Classify this cell by malaria status.
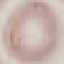
Uninfected.

{
  "stain": "Giemsa",
  "preparation": "thin blood film",
  "capture": "smartphone through the microscope eyepiece",
  "image_type": "cell patch, automatically extracted from a larger field of view and resized to 64 × 64 pixels"
}